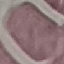

Summary:
  - Malaria status: uninfected
  - Stain: Giemsa
  - Preparation: thin blood smear
  - Image type: automatically extracted cell patch, resized to 64 × 64 pixels
  - Capture: smartphone through the microscope eyepiece